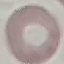
Malaria status: uninfected. Acquired by smartphone through the microscope eyepiece. Automatically extracted cell patch, resized to 64 × 64 pixels. Thin blood film. Giemsa-stained preparation.